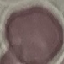 Malaria status: uninfected. Giemsa stain. Acquired by smartphone through the microscope eyepiece. Thin blood smear. Automatically extracted cell patch, resized to 64 × 64 pixels.